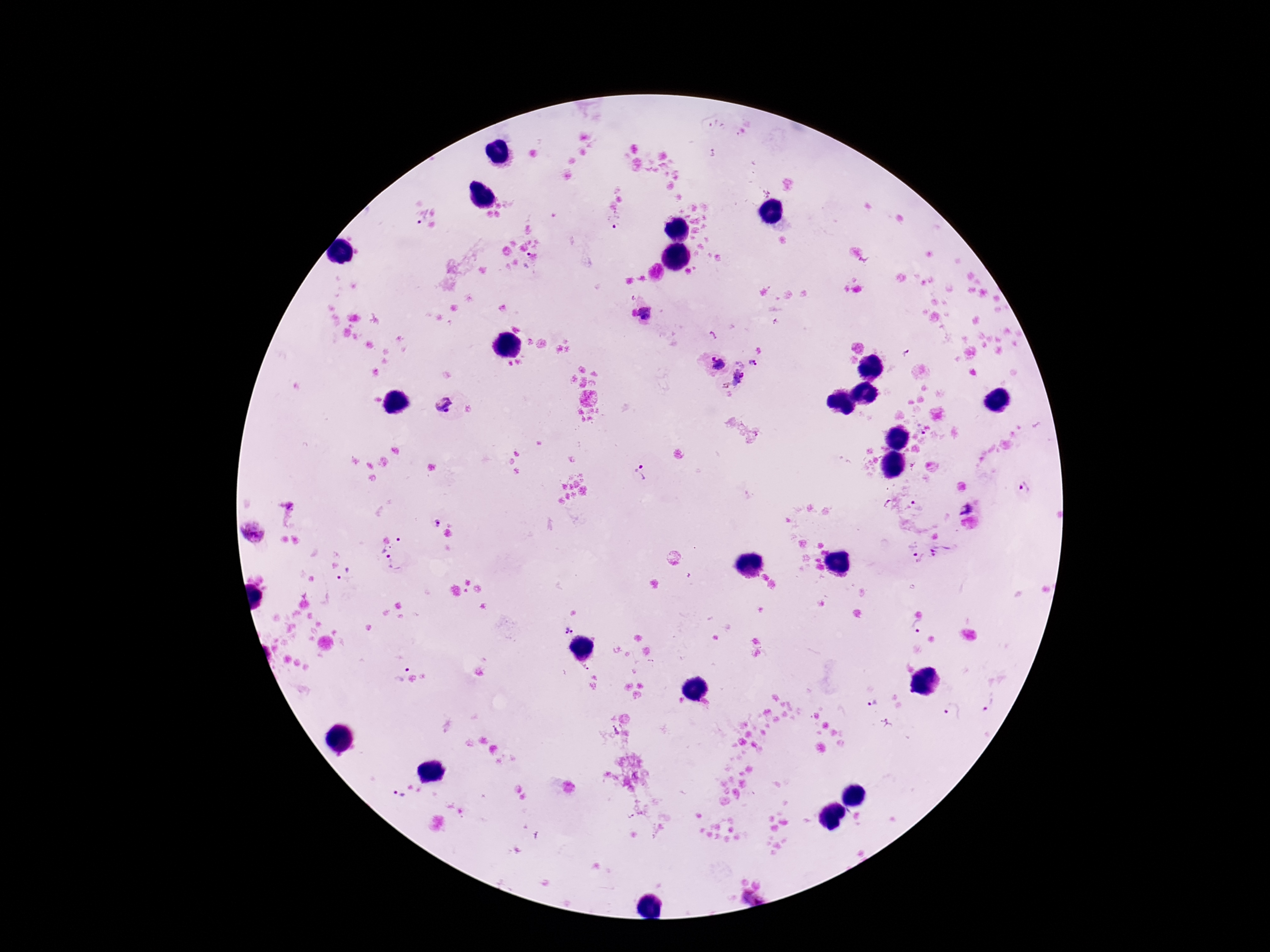

Approximate object centers, in pixels from the top-left corner.
Summary:
  - Plasmodium parasite locations: (x=421, y=217), (x=615, y=221), (x=527, y=260), (x=648, y=313), (x=907, y=353), (x=754, y=362), (x=716, y=363), (x=733, y=375), (x=443, y=406), (x=922, y=433), (x=641, y=473), (x=1025, y=487), (x=291, y=504), (x=919, y=505), (x=964, y=508), (x=435, y=521), (x=252, y=531), (x=398, y=538), (x=382, y=549), (x=940, y=551), (x=918, y=556), (x=394, y=562), (x=346, y=577), (x=568, y=627), (x=915, y=628), (x=586, y=668), (x=399, y=669), (x=872, y=701), (x=991, y=701), (x=953, y=713), (x=399, y=799), (x=751, y=897)
  - Magnification: 100x
  - Stain: Giemsa
  - Capture: smartphone camera through the microscope eyepiece
  - Field of view: single
  - Patient malaria status: positive
  - Image size: 1270×952 pixels
  - Preparation: thick blood smear